State the preparation type.
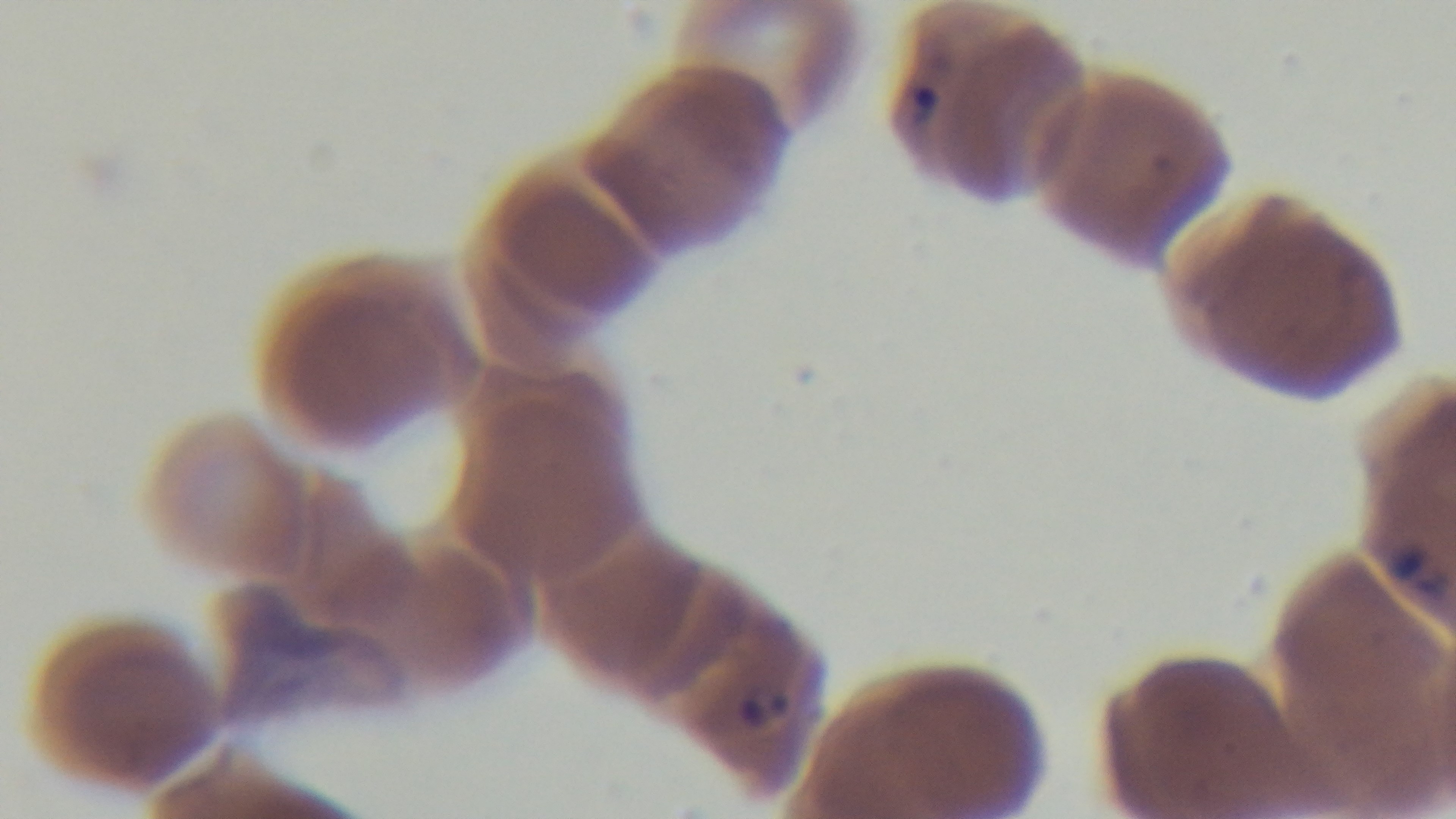

It is a thin blood film.

field of view = one from the slide
capture = mounted 4K digital camera
malaria status = infected
modality = light microscopy
stain = Giemsa
objective = 100x oil immersion